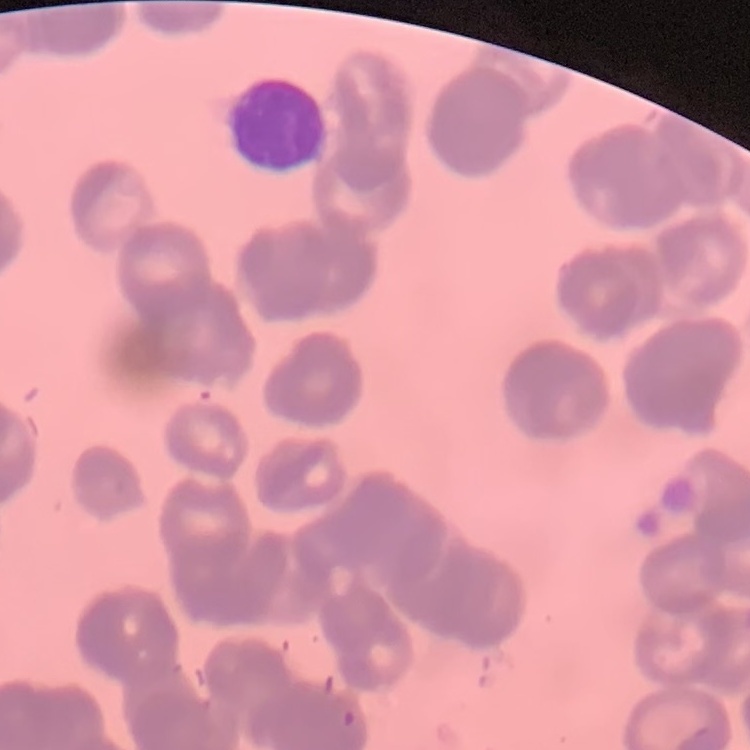

{
  "erythrocyte_morphology": "rouleaux formation",
  "stain": "Field's or Giemsa",
  "preparation": "thin blood film",
  "image_type": "square crop of a larger photomicrograph"
}